Locate platelets.
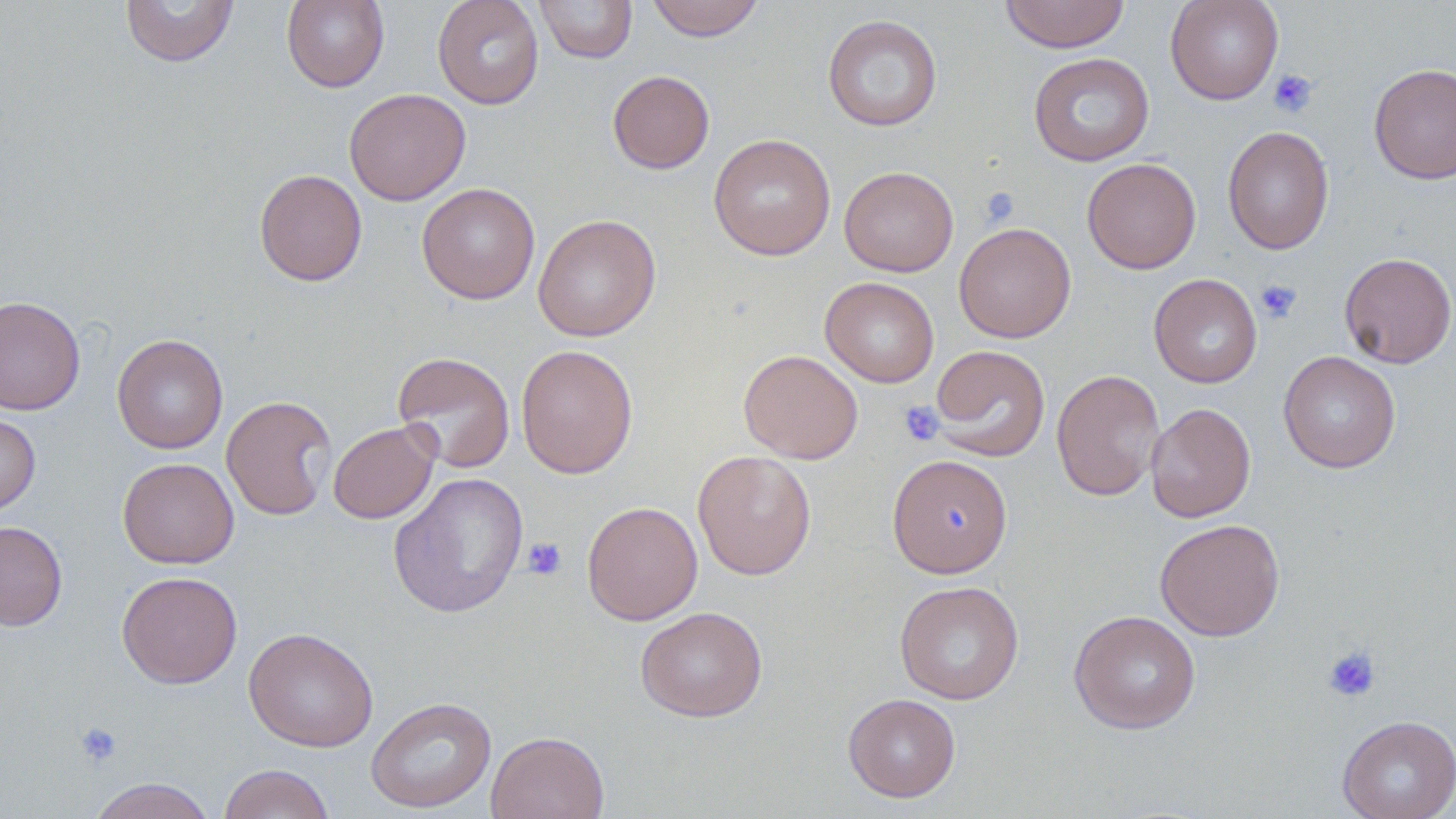
Approximate bounding boxes as (x1, y1, x2, y2) in pixels.
Platelets: (1268, 69, 1318, 118), (980, 187, 1019, 226), (1255, 279, 1302, 323), (899, 401, 944, 446), (521, 536, 567, 580), (1321, 645, 1381, 703), (74, 721, 123, 768).

Uninfected red blood cell locations: (120, 0, 239, 67), (281, 0, 389, 92), (432, 0, 545, 110), (534, 0, 638, 64), (646, 0, 765, 41), (998, 0, 1130, 53), (1165, 0, 1283, 105), (822, 14, 943, 132), (1028, 52, 1154, 167), (1368, 63, 1456, 184), (607, 70, 714, 174), (344, 88, 471, 206), (1222, 125, 1334, 255), (708, 134, 836, 260), (1082, 157, 1201, 274), (839, 166, 959, 276), (254, 169, 368, 286), (416, 183, 540, 304), (533, 213, 661, 341), (953, 222, 1076, 344), (1339, 252, 1456, 368), (1149, 273, 1263, 388), (820, 277, 939, 388), (0, 295, 85, 416), (112, 333, 228, 454), (516, 344, 638, 478), (930, 345, 1051, 461), (738, 349, 863, 464), (1278, 350, 1401, 473), (392, 351, 515, 473), (1051, 369, 1165, 502), (221, 394, 337, 521), (1145, 403, 1256, 523), (0, 412, 41, 515), (328, 421, 439, 524), (692, 450, 817, 580), (887, 454, 1013, 577), (117, 457, 239, 569), (388, 471, 529, 618), (582, 501, 703, 625), (1155, 518, 1285, 641), (0, 521, 68, 631), (116, 571, 242, 689), (894, 581, 1025, 705), (635, 606, 768, 722), (1069, 609, 1200, 734), (244, 627, 378, 752), (842, 693, 961, 802), (365, 696, 497, 813), (1337, 714, 1456, 819), (486, 730, 609, 819), (218, 763, 336, 819), (87, 777, 217, 819). Slide-level diagnosis: negative for blood parasites. Thin blood smear. Image is 1456×819 pixels. Optical microscopy. May-Grünwald-Giemsa stain. Captured at 1000x magnification. Single field of view.